Classify this cell by malaria status.
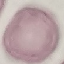

Uninfected.

{
  "stain": "Giemsa",
  "capture": "smartphone camera at the microscope eyepiece",
  "image_type": "automatically extracted cell patch, resized to 64 × 64 pixels",
  "preparation": "thin blood smear"
}